Report the malaria status.
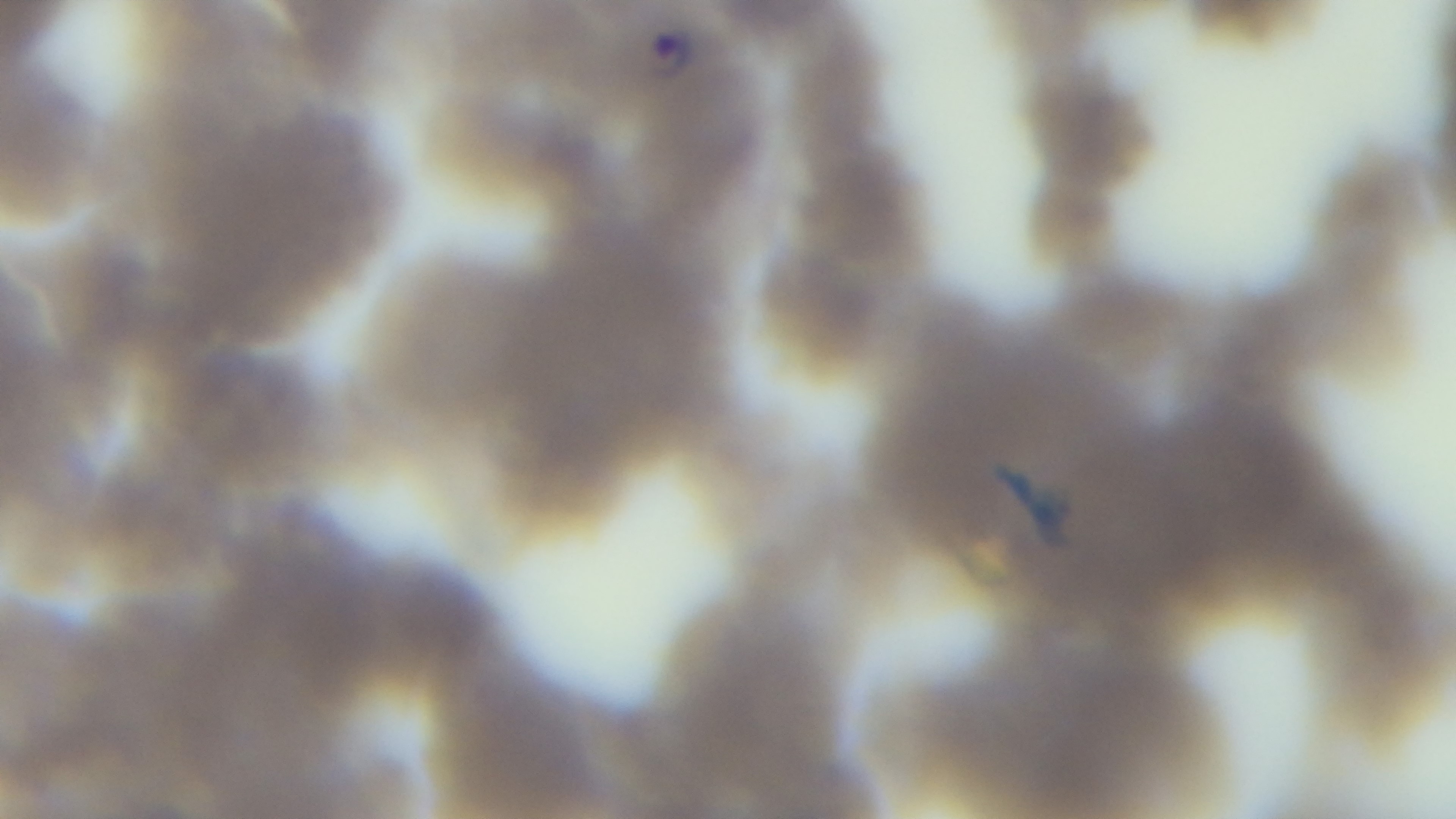
Positive.

Summary:
  - Stain: Giemsa
  - Modality: light microscopy
  - Capture: mounted 4K digital camera
  - Preparation: thin smear
  - Objective: 100x oil immersion
  - Field of view: one from the slide